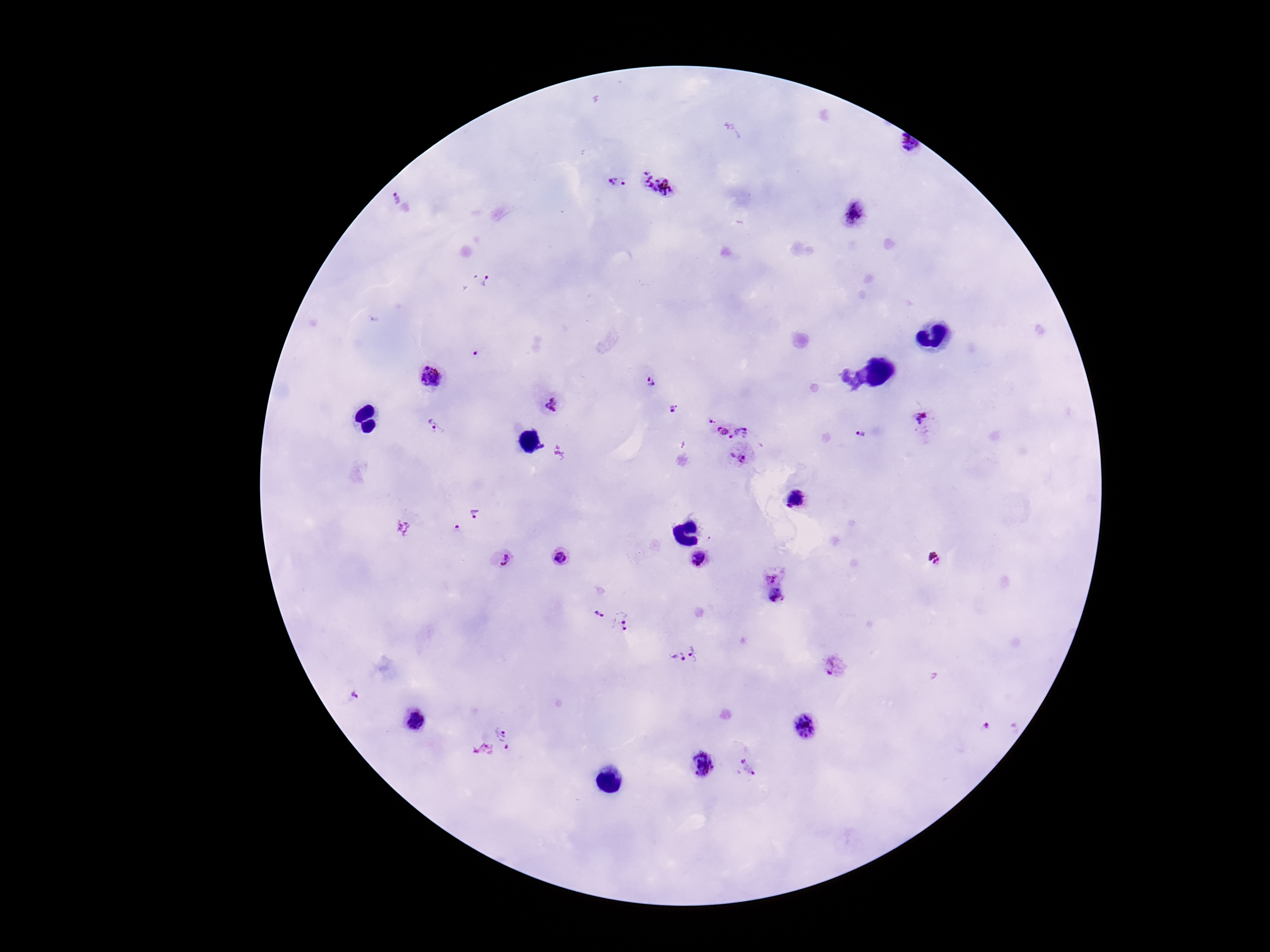

stain = Giemsa
image size = 1270×952 pixels
preparation = thick peripheral-blood smear
magnification = 100x
field of view = single
patient malaria status = positive
Plasmodium parasite locations = approximate centers as {x, y} in pixels: {907, 148}, {617, 184}, {659, 184}, {397, 194}, {854, 213}, {487, 283}, {474, 352}, {431, 377}, {651, 382}, {550, 405}, {673, 409}, {710, 421}, {926, 421}, {437, 427}, {722, 431}, {740, 432}, {860, 434}, {730, 437}, {739, 456}, {798, 499}, {475, 514}, {458, 530}, {559, 558}, {935, 558}, {501, 559}, {699, 560}, {776, 575}, {777, 597}, {599, 616}, {625, 623}, {697, 654}, {675, 659}, {833, 666}, {355, 696}, {415, 722}, {987, 726}, {804, 728}, {492, 744}, {701, 766}, {748, 768}
capture = smartphone camera through the microscope eyepiece